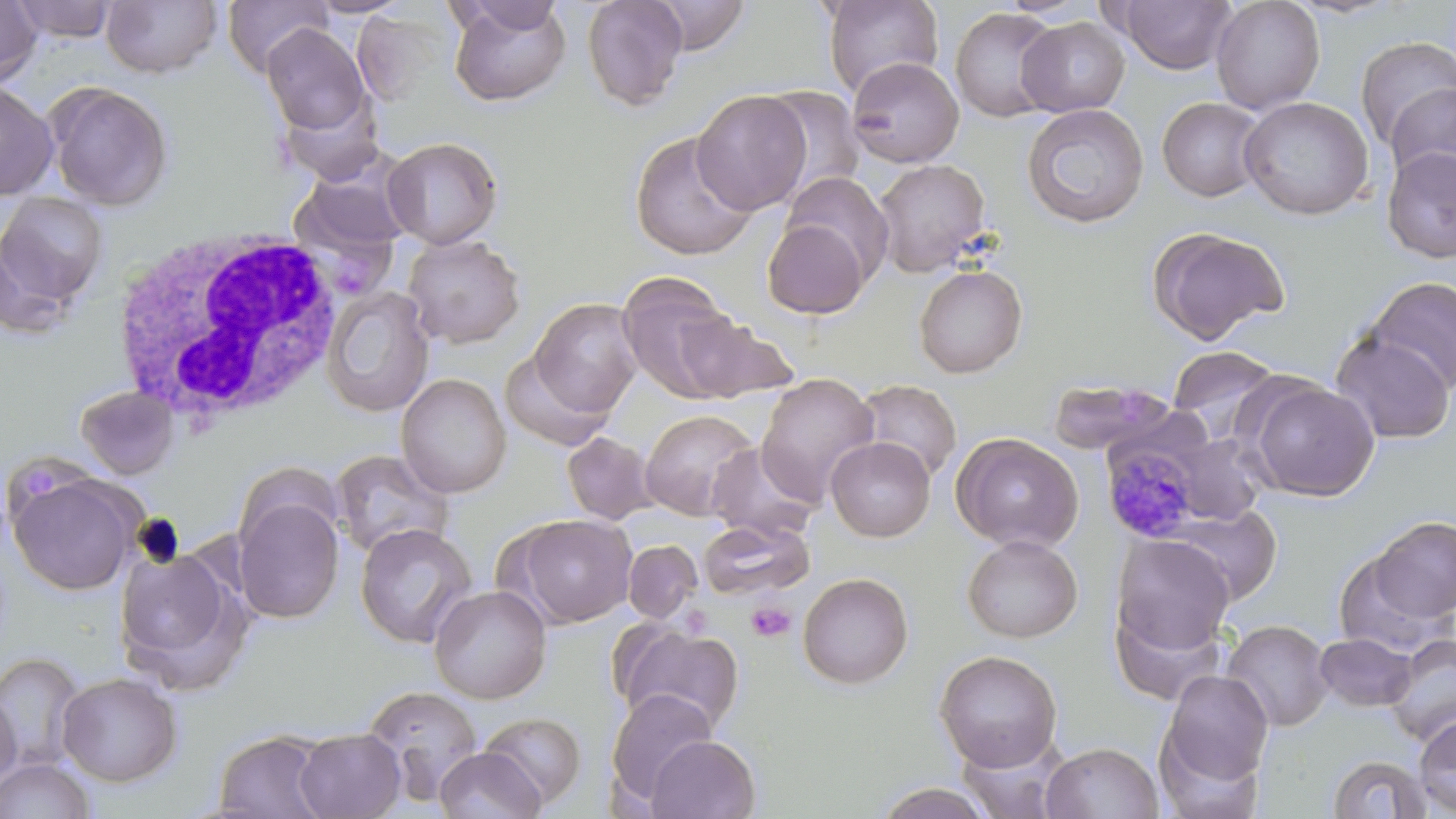
{
  "slide_level_diagnosis": "Plasmodium malariae",
  "image_size": "1456×819 pixels",
  "modality": "light microscopy",
  "uninfected_red_blood_cell_locations": "approximate bounding boxes as (x1,y1)-(x2,y2) corner pairs in pixels: (0,0)-(43,88), (10,0)-(118,43), (221,0)-(332,78), (305,0)-(413,18), (448,0)-(571,107), (581,0)-(689,111), (647,0)-(753,55), (820,0)-(944,98), (1116,0)-(1236,74), (1210,0)-(1326,115), (1281,0)-(1408,19), (101,1)-(223,78), (949,7)-(1061,123), (1016,17)-(1130,117), (261,24)-(372,137), (1354,35)-(1456,151), (847,56)-(964,168), (0,80)-(59,201), (44,81)-(174,211), (1385,81)-(1456,192), (760,86)-(865,198), (692,89)-(812,215), (276,94)-(385,184), (1238,95)-(1375,220), (1157,97)-(1268,202), (1021,103)-(1149,229), (628,131)-(760,261), (381,136)-(503,249), (1380,146)-(1456,264), (292,157)-(414,257), (872,158)-(992,277), (781,172)-(892,280), (0,192)-(109,310), (762,217)-(869,319), (1147,226)-(1290,345), (402,234)-(526,348), (913,264)-(1028,378), (616,273)-(746,403), (1365,276)-(1456,394), (320,286)-(435,418), (529,298)-(642,417), (673,312)-(799,403), (1329,331)-(1455,445), (1168,345)-(1282,442), (499,351)-(615,452), (395,373)-(512,498), (755,373)-(880,507), (1046,377)-(1177,456), (1246,378)-(1378,502), (855,379)-(962,483), (75,385)-(180,479), (640,409)-(759,521), (950,431)-(1085,552), (1167,431)-(1268,525), (561,432)-(658,525), (825,437)-(935,542), (707,443)-(820,542), (329,448)-(454,560), (234,461)-(343,558), (6,466)-(144,596), (232,493)-(345,624), (508,513)-(637,628), (1371,516)-(1456,621), (697,518)-(813,601), (355,523)-(477,649), (1110,533)-(1235,658), (961,534)-(1084,643), (623,540)-(703,623), (113,545)-(251,694), (1334,549)-(1451,659), (797,572)-(914,689), (429,584)-(552,704), (1109,600)-(1229,706), (1221,619)-(1334,731), (613,621)-(746,736), (1314,633)-(1418,711), (1384,634)-(1455,746), (934,649)-(1063,772), (0,651)-(87,774), (1159,670)-(1273,787), (57,672)-(183,787), (361,686)-(484,803), (605,687)-(718,804), (0,689)-(21,791), (477,711)-(587,810), (1413,714)-(1456,814), (293,728)-(406,818), (213,730)-(335,818), (645,734)-(760,818), (1041,741)-(1163,819), (435,747)-(546,819), (1327,754)-(1433,818), (0,756)-(96,818), (870,781)-(999,817)",
  "preparation": "thin blood smear",
  "platelet_locations": "approximate bounding boxes as (x1,y1)-(x2,y2) corner pairs in pixels: (20,468)-(62,503), (746,600)-(796,643)",
  "magnification": "1000x",
  "field_of_view": "single",
  "white_blood_cell_locations": "approximate bounding boxes as (x1,y1)-(x2,y2) corner pairs in pixels: (111,229)-(344,431)",
  "stain": "May-Grünwald-Giemsa",
  "plasmodium_malariae_infected_red_blood_cell_locations": "approximate bounding boxes as (x1,y1)-(x2,y2) corner pairs in pixels: (1101,437)-(1208,543)"
}